Comment on the morphology of the red blood cells.
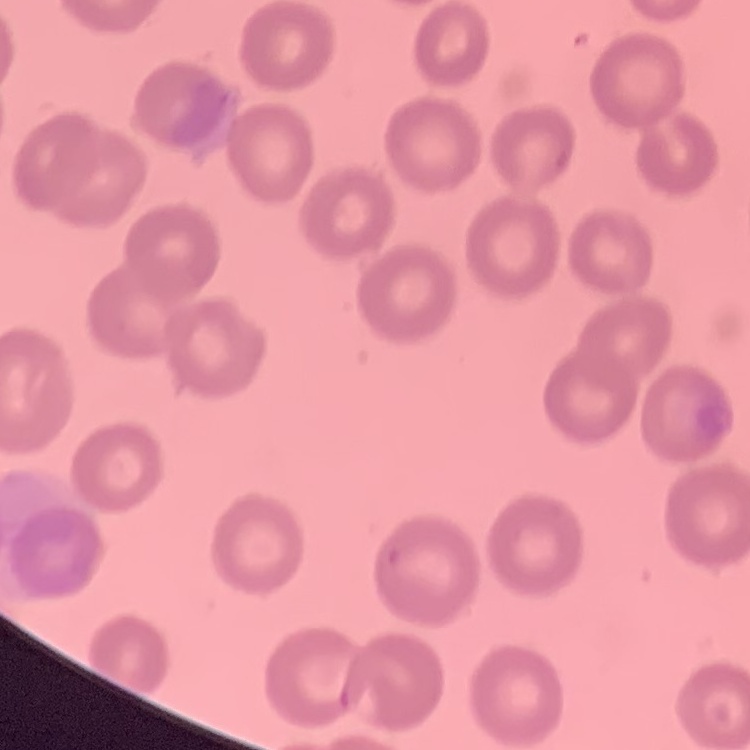

No rouleaux formation.

Summary:
  - Stain: Field's or Giemsa
  - Image type: one tile cut from a larger photomicrograph
  - Preparation: thin peripheral smear